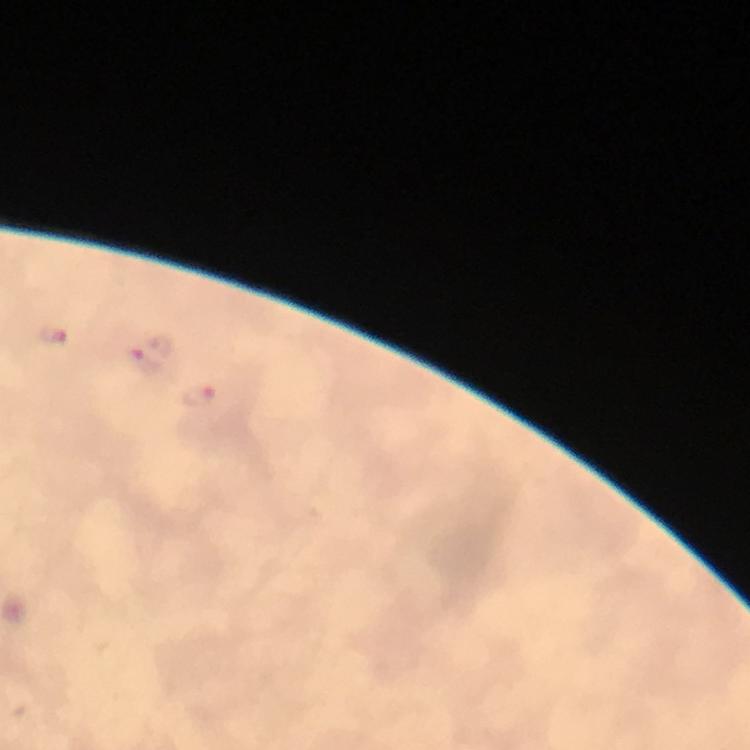
image size = 750×750 pixels
preparation = thick blood film
capture = smartphone mounted on the microscope
cropped from = one field of view
magnification = 100x
immersion oil = applied
Plasmodium parasite locations = approximate centers as (x, y) in pixels: (52, 336), (142, 364), (199, 395)
stain = Giemsa
context = from a diagnostic examination for malaria